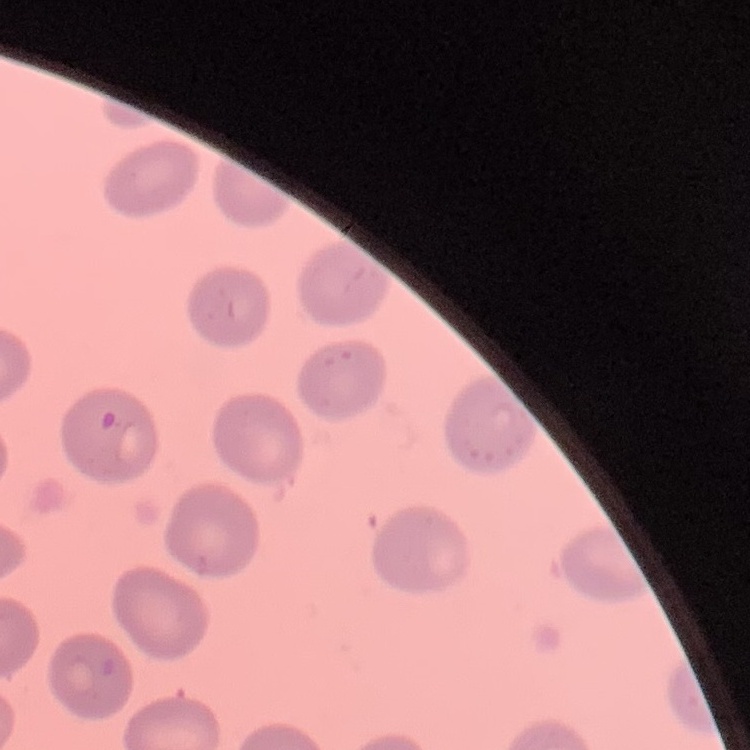

The erythrocytes exhibit no rouleaux formation. One tile cut from a larger photomicrograph. Field's or Giemsa stain. Thin blood film.